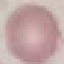

Summary:
  - Result: negative for malaria parasites
  - Stain: Giemsa
  - Image type: cell patch, automatically extracted from a larger field of view and resized to 64 × 64 pixels
  - Preparation: thin smear
  - Capture: smartphone through the microscope eyepiece